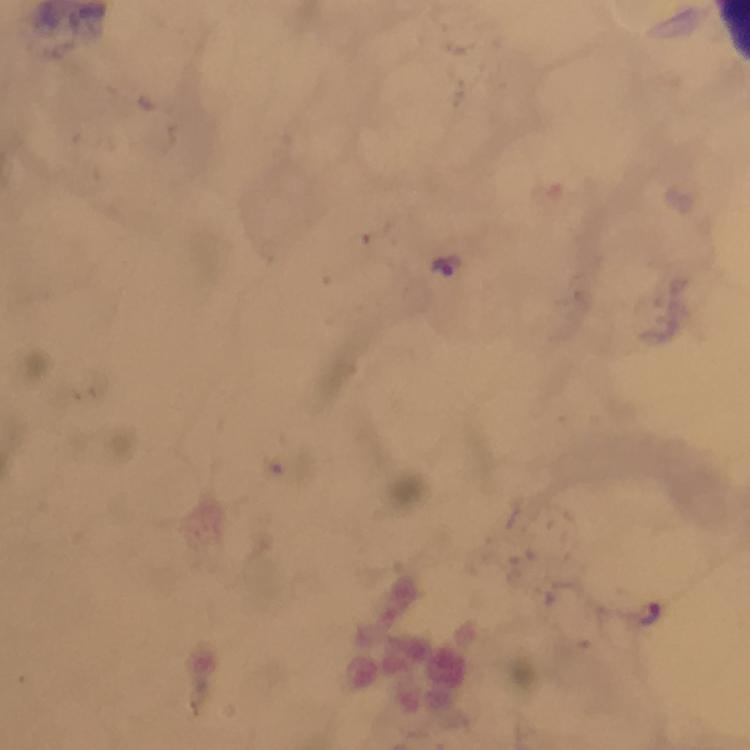 Approximate centers as {x, y} in pixels. Plasmodium parasite locations: {446, 265}, {649, 615}. Giemsa-stained preparation. Thick smear. A crop from one field of view. Image is 750×750 pixels. Photographed with a smartphone mounted on the microscope. Immersion oil was used. From a diagnostic examination for malaria. At 100x magnification.